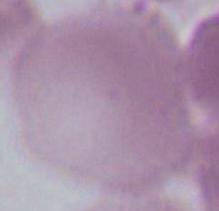
identification: erythrocyte
modality: micrograph
magnification: 1000x